Outline each Plasmodium falciparum-infected red blood cell.
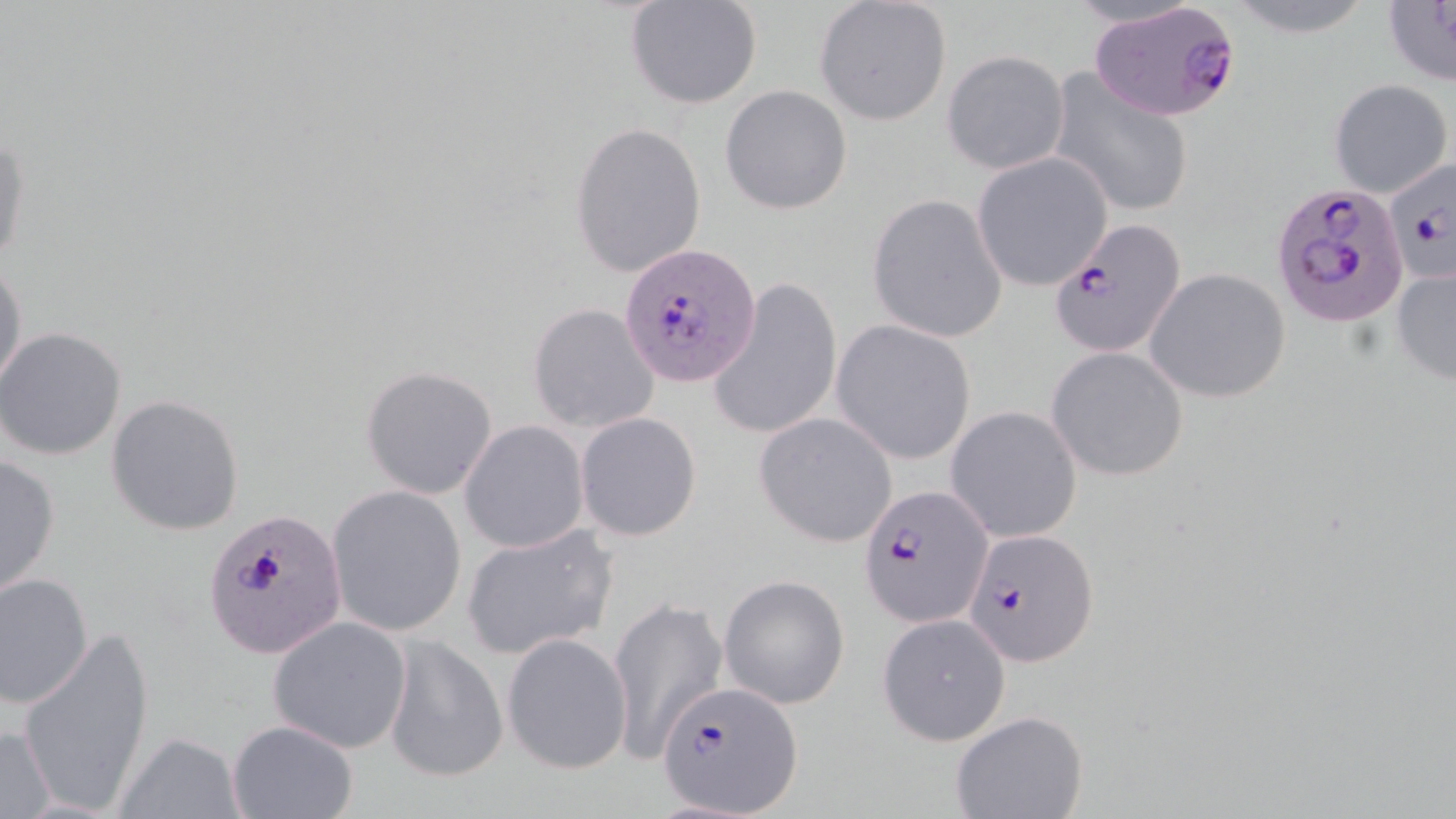
Approximate bounding boxes as [x1, y1, x2, y2] in pixels.
Plasmodium falciparum-infected red blood cells: [1089, 1, 1242, 122], [1384, 156, 1456, 286], [1276, 182, 1411, 328], [1050, 219, 1187, 361], [621, 240, 762, 388], [860, 485, 991, 627], [205, 506, 347, 660], [964, 527, 1099, 667], [657, 679, 802, 814].

Uninfected red blood cell locations: [1224, 0, 1377, 37], [1380, 0, 1456, 89], [624, 1, 762, 111], [813, 2, 953, 125], [942, 51, 1070, 174], [1046, 69, 1196, 217], [1327, 78, 1454, 198], [720, 85, 853, 215], [570, 121, 706, 280], [0, 129, 30, 273], [971, 150, 1115, 290], [867, 194, 1008, 343], [0, 257, 27, 395], [1391, 262, 1456, 386], [1143, 268, 1291, 404], [709, 276, 842, 441], [527, 304, 659, 433], [830, 321, 977, 464], [0, 327, 128, 461], [1047, 346, 1190, 482], [360, 365, 498, 500], [106, 394, 245, 537], [945, 404, 1083, 543], [576, 411, 702, 541], [755, 412, 898, 548], [461, 420, 588, 552], [0, 453, 62, 600], [326, 485, 467, 637], [461, 524, 618, 659], [1, 573, 94, 708], [718, 574, 851, 709], [608, 598, 727, 764], [876, 613, 1012, 747], [267, 617, 412, 752], [16, 624, 156, 815], [502, 632, 633, 774], [384, 636, 507, 784], [950, 711, 1088, 819], [226, 719, 359, 819], [0, 724, 56, 817], [116, 732, 246, 817]. Slide-level diagnosis: Plasmodium falciparum. May-Grünwald-Giemsa stain. Thin blood smear. 1000x magnification. Optical microscopy. Image is 1456×819 pixels. Single field of view.